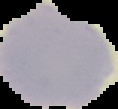 Result: negative for malaria parasites. Cell region segmented out of the field of view; the surrounding area is masked to black. From a thin blood smear. Image is 118×109 pixels.